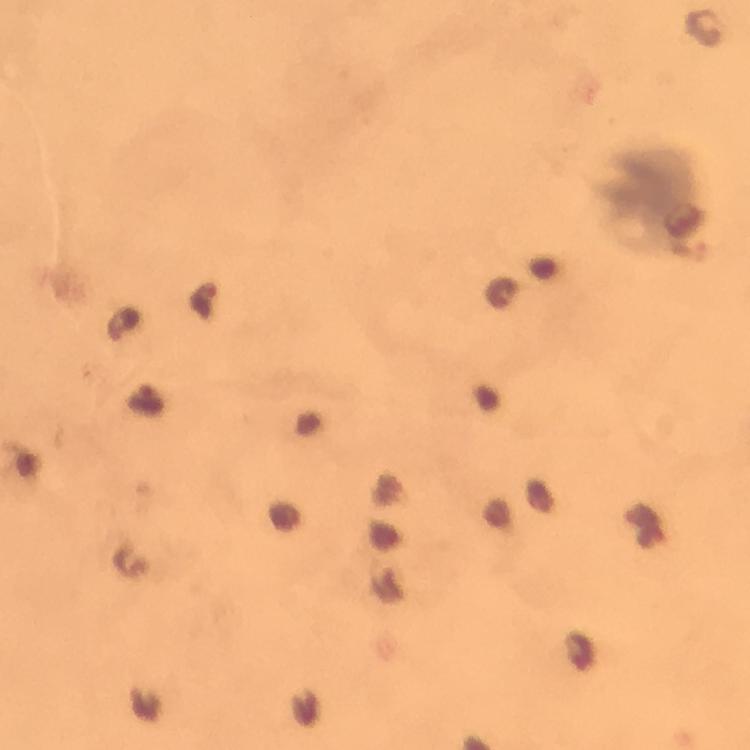
context = from a diagnostic examination for malaria
preparation = thick blood smear
immersion oil = applied
cropped from = one field of view
stain = Giemsa
capture = smartphone camera through the microscope
magnification = 100x
Plasmodium parasite locations = approximate object centers, in pixels from the top-left corner: (x=204, y=299), (x=123, y=323), (x=145, y=400)
image size = 750×750 pixels